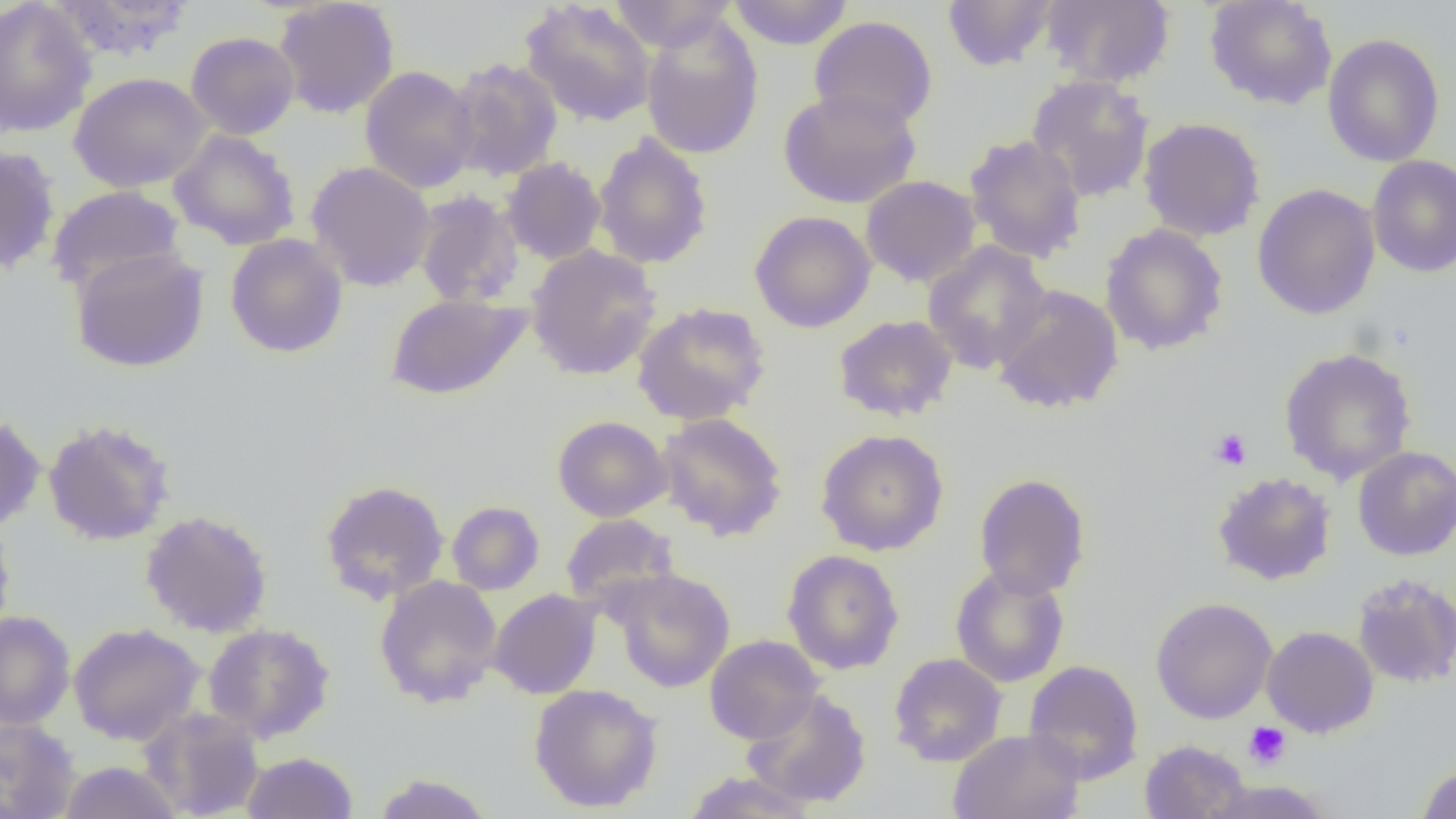

slide-level diagnosis = no evidence of blood parasites
uninfected red blood cell locations = approximate bounding boxes as [x1, y1, x2, y2] in pixels: [49, 0, 196, 62], [608, 0, 737, 52], [726, 0, 855, 50], [942, 0, 1059, 72], [1040, 0, 1174, 88], [1204, 0, 1338, 110], [0, 1, 97, 137], [273, 1, 400, 118], [519, 1, 657, 127], [640, 15, 764, 160], [809, 15, 938, 131], [186, 31, 300, 139], [1322, 32, 1445, 167], [445, 57, 564, 182], [360, 65, 480, 193], [69, 72, 210, 193], [1026, 74, 1154, 203], [777, 87, 921, 209], [1138, 117, 1266, 241], [168, 129, 301, 250], [593, 132, 713, 270], [963, 134, 1088, 263], [0, 145, 61, 275], [1366, 154, 1456, 278], [501, 157, 607, 265], [306, 161, 435, 291], [860, 175, 981, 287], [46, 184, 185, 294], [1252, 184, 1380, 320], [413, 189, 525, 308], [749, 210, 876, 333], [1100, 223, 1228, 355], [225, 233, 348, 358], [922, 241, 1052, 373], [525, 244, 662, 381], [69, 247, 209, 373], [991, 284, 1124, 414], [385, 293, 531, 401], [631, 302, 771, 426], [832, 314, 958, 422], [1278, 347, 1418, 484], [657, 412, 788, 541], [0, 413, 46, 533], [552, 416, 672, 522], [42, 417, 176, 546], [815, 429, 949, 556], [1352, 446, 1456, 560], [1212, 471, 1337, 585], [973, 472, 1091, 599], [319, 479, 450, 605], [447, 501, 545, 595], [140, 509, 274, 637], [561, 513, 680, 611], [0, 519, 16, 642], [782, 549, 904, 675], [950, 564, 1070, 688], [611, 568, 736, 693], [1351, 572, 1455, 689], [374, 576, 502, 708], [488, 589, 602, 699], [1150, 597, 1277, 724], [0, 611, 75, 729], [68, 622, 204, 745], [202, 623, 336, 744], [1261, 626, 1379, 737], [704, 635, 824, 745], [888, 653, 1007, 767], [1023, 659, 1144, 784], [528, 683, 663, 813], [742, 689, 872, 808], [138, 707, 266, 819], [0, 718, 80, 819], [948, 728, 1086, 819], [1139, 740, 1251, 819], [240, 751, 359, 818], [57, 760, 184, 819], [1414, 763, 1456, 819], [679, 771, 822, 817], [370, 773, 496, 819], [1207, 778, 1333, 819]
platelet locations = approximate bounding boxes as [x1, y1, x2, y2] in pixels: [1209, 428, 1251, 470], [1244, 722, 1291, 769]
field of view = single
preparation = thin blood film
magnification = 1000x
image size = 1456×819 pixels
modality = optical microscopy